Identify the cell.
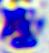

A leukocyte.

Summary:
  - Modality: photomicrograph
  - Magnification: 400x